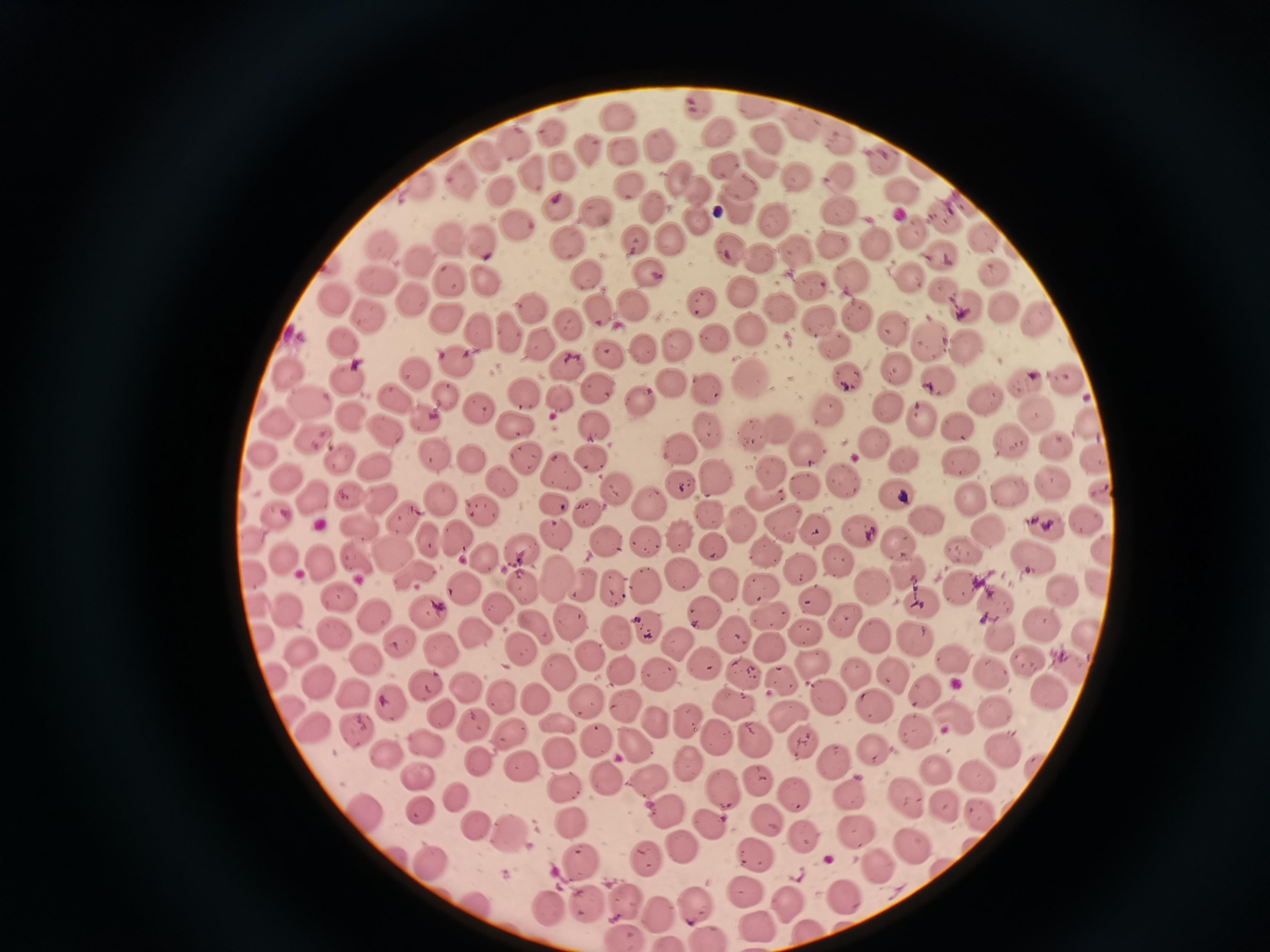

Approximate centers as [x, y] in pixels. Cell locations: [697, 105], [755, 105], [616, 117], [803, 125], [718, 132], [550, 133], [840, 136], [768, 138], [514, 144], [660, 144], [588, 148], [622, 151], [484, 155], [882, 157], [764, 163], [559, 167], [724, 167], [529, 172], [679, 174], [839, 175], [797, 176], [461, 182], [420, 187], [497, 187], [903, 187], [627, 188], [742, 188], [699, 190], [554, 208], [596, 210], [840, 210], [652, 211], [947, 217], [696, 219], [773, 220], [518, 222], [914, 229], [984, 234], [448, 237], [670, 239], [633, 240], [382, 241], [564, 242], [836, 242], [876, 242], [485, 243], [729, 249], [797, 254], [940, 255], [760, 258], [421, 262], [649, 272], [993, 272], [909, 274], [849, 275], [588, 276], [449, 279], [485, 279], [378, 280], [811, 285], [745, 290], [943, 291], [336, 298], [414, 298], [699, 302], [635, 304], [964, 305], [780, 307], [1002, 309], [601, 311], [532, 312], [856, 313], [373, 315], [1038, 317], [819, 319], [447, 320], [568, 321], [891, 328], [749, 329], [483, 330], [509, 335], [713, 338], [929, 339], [539, 342], [675, 343], [836, 344], [342, 345], [967, 346], [639, 349], [606, 352], [453, 362], [566, 367], [897, 368], [285, 371], [414, 374], [845, 374], [938, 377], [749, 379], [1061, 379], [347, 380], [670, 381], [1023, 383], [597, 386], [704, 389], [443, 396], [525, 396], [987, 398], [562, 399], [395, 400], [639, 400], [306, 401], [479, 409], [887, 409], [827, 411], [1035, 414], [348, 415], [425, 416], [916, 420], [278, 426], [518, 426], [382, 427], [596, 427], [956, 427], [1088, 428], [779, 429], [708, 432], [746, 433], [313, 435], [871, 441], [1007, 441], [1054, 444], [678, 446], [807, 450], [436, 452], [263, 453], [525, 455], [1096, 457], [471, 459], [903, 459], [959, 461], [593, 462], [340, 463], [372, 466], [558, 471], [767, 472], [712, 477], [841, 479], [1054, 480], [286, 482], [503, 483], [682, 487], [803, 488], [1102, 490], [619, 491], [1011, 493], [344, 494], [896, 495], [312, 496], [970, 496], [439, 497], [381, 498], [761, 498], [555, 503], [477, 507], [649, 507], [583, 509], [273, 511], [708, 513], [403, 517], [781, 520], [1086, 520], [928, 522], [1047, 522], [739, 523], [356, 527], [817, 530], [856, 531], [988, 532], [558, 535], [455, 536], [679, 536], [426, 537], [899, 539], [606, 541], [643, 541], [711, 546], [1099, 549], [766, 552], [963, 553], [396, 554], [521, 555], [1033, 556], [482, 557], [319, 559], [837, 559], [285, 561], [359, 562], [801, 573], [418, 574], [682, 574], [556, 575], [1095, 578], [582, 581], [517, 584], [645, 585], [615, 586], [963, 586], [723, 587], [872, 587], [464, 588], [759, 589], [1065, 589], [343, 598], [813, 598], [998, 604], [922, 607], [286, 609], [704, 609], [498, 610], [372, 611], [769, 612], [428, 614], [846, 621], [568, 623], [1038, 624], [651, 626], [615, 628], [536, 629], [478, 631], [1077, 631], [335, 634], [807, 635], [1003, 637], [916, 638], [735, 639], [874, 639], [674, 645], [398, 646], [438, 646], [764, 648], [297, 649], [521, 649], [590, 655], [366, 657], [1024, 658], [952, 663], [1067, 663], [703, 665], [815, 668], [618, 669], [558, 671], [743, 671], [854, 671], [992, 672], [891, 673], [658, 676], [786, 680], [424, 684], [323, 686], [465, 689], [1050, 692], [829, 696], [351, 697], [502, 697], [537, 698], [581, 700], [736, 703], [389, 704], [622, 706], [877, 706], [443, 713], [794, 714], [996, 715], [949, 717], [690, 719], [655, 722], [316, 723], [561, 724], [473, 727], [508, 730], [916, 730], [719, 736], [759, 738], [805, 739], [596, 740], [427, 744], [632, 744], [875, 749], [388, 752], [999, 752], [562, 756], [689, 759], [479, 761], [834, 761], [932, 768], [520, 769], [420, 775], [605, 776], [975, 776], [758, 778], [649, 780], [567, 789], [722, 789], [851, 791], [792, 794], [460, 796], [907, 798], [944, 804], [366, 810], [423, 811], [979, 813], [669, 815], [766, 818], [572, 821], [478, 824], [709, 824], [857, 829], [512, 835], [801, 836], [684, 845], [912, 845], [756, 853], [646, 854], [579, 861], [877, 863], [433, 864], [748, 894], [841, 894], [625, 901], [583, 902], [691, 903], [783, 903], [552, 906], [658, 910], [753, 923], [806, 932], [622, 936], [707, 937], [668, 942]. Photographed with a smartphone camera at the microscope eyepiece. Single field of view. Giemsa-stained preparation. Image is 1270×952 pixels. Thin blood film.